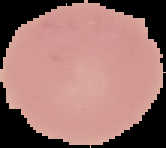 Malaria status: uninfected. Image is 166×148 pixels. Segmented cell region on a black background. From a thin blood smear.